State which parasite is depicted.
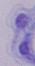

A trypanosome.

1000x magnification. Micrograph.